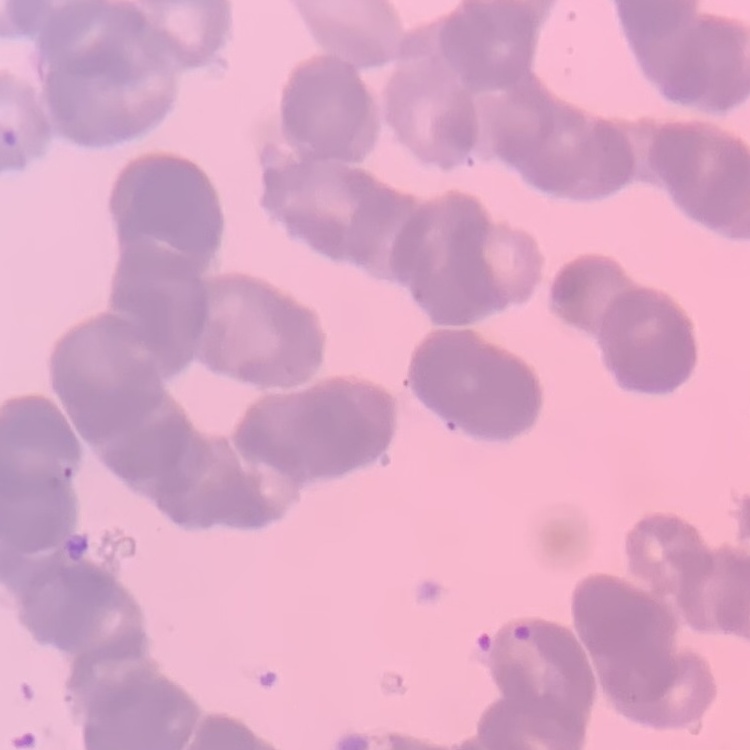

Summary:
  - Erythrocyte morphology: rouleaux formation
  - Preparation: thin blood smear
  - Image type: square crop of a larger photomicrograph
  - Stain: Field's or Giemsa